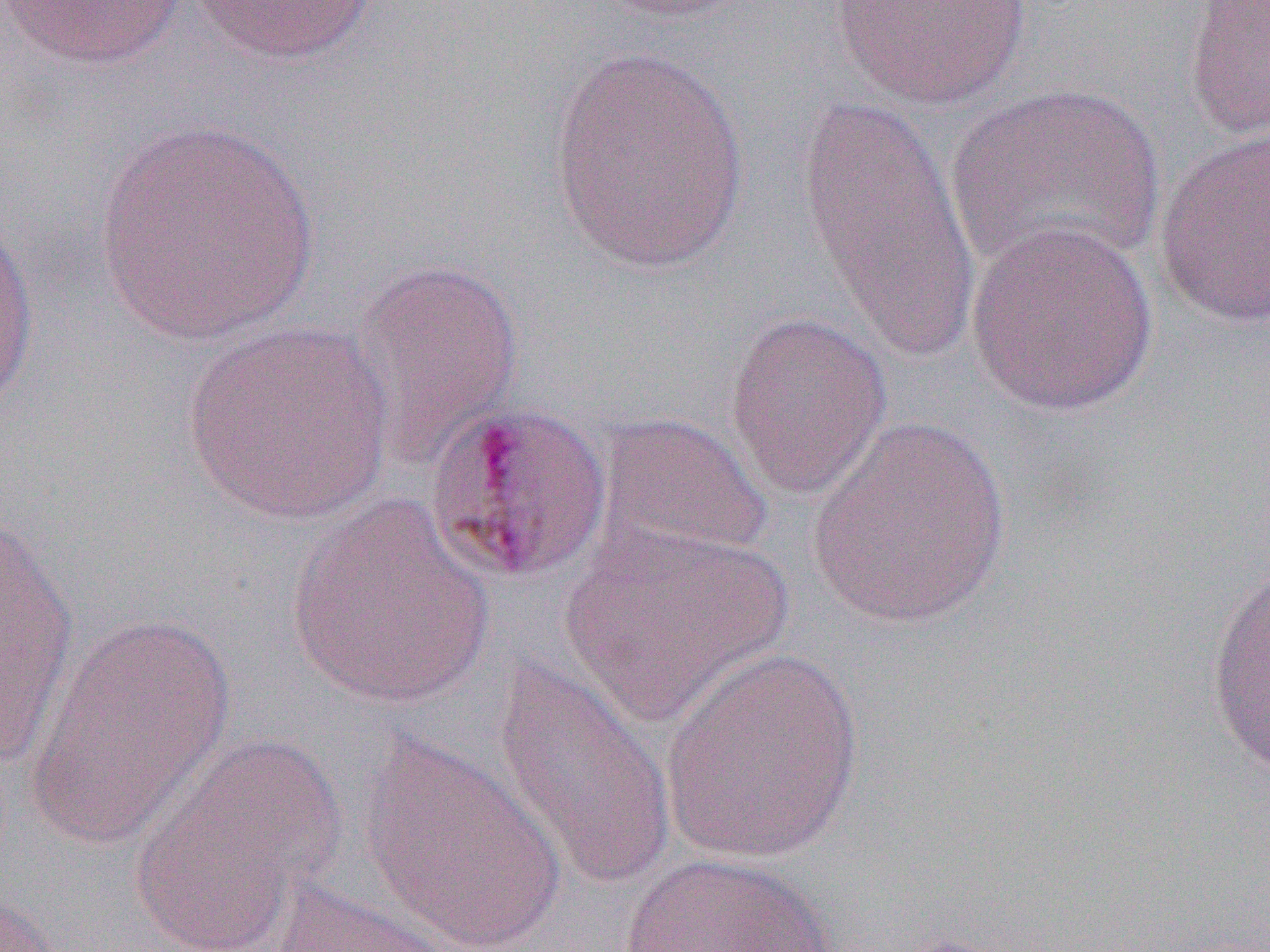

Summary:
  - Coordinate format: approximate bounding boxes as (x1, y1, x2, y2) in pixels
  - Uninfected red blood cell locations: (2, 0, 192, 70), (188, 0, 379, 65), (592, 0, 757, 24), (828, 0, 1030, 110), (1181, 1, 1269, 144), (547, 43, 753, 278), (946, 83, 1166, 281), (795, 95, 984, 363), (93, 117, 320, 346), (1152, 126, 1270, 330), (0, 210, 40, 418), (964, 218, 1160, 417), (348, 258, 525, 468), (723, 309, 892, 501), (180, 321, 397, 525), (594, 411, 775, 564), (805, 416, 1012, 629), (281, 495, 497, 710), (0, 513, 80, 764), (560, 521, 793, 724), (1204, 566, 1270, 776), (25, 614, 236, 851), (660, 646, 865, 863), (490, 656, 677, 888), (128, 733, 343, 949), (357, 733, 569, 950), (619, 851, 844, 952), (265, 880, 460, 952), (0, 884, 68, 951)
  - Slide-level diagnosis: Plasmodium malariae
  - Magnification: 1000x
  - Modality: optical microscopy
  - Field of view: single
  - Image size: 1270×952 pixels
  - Preparation: thin blood smear